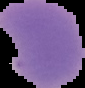

image type = segmented cell region on a black background
image size = 85×88 pixels
preparation = thin blood film
malaria status = parasitized